Point out every malaria parasite.
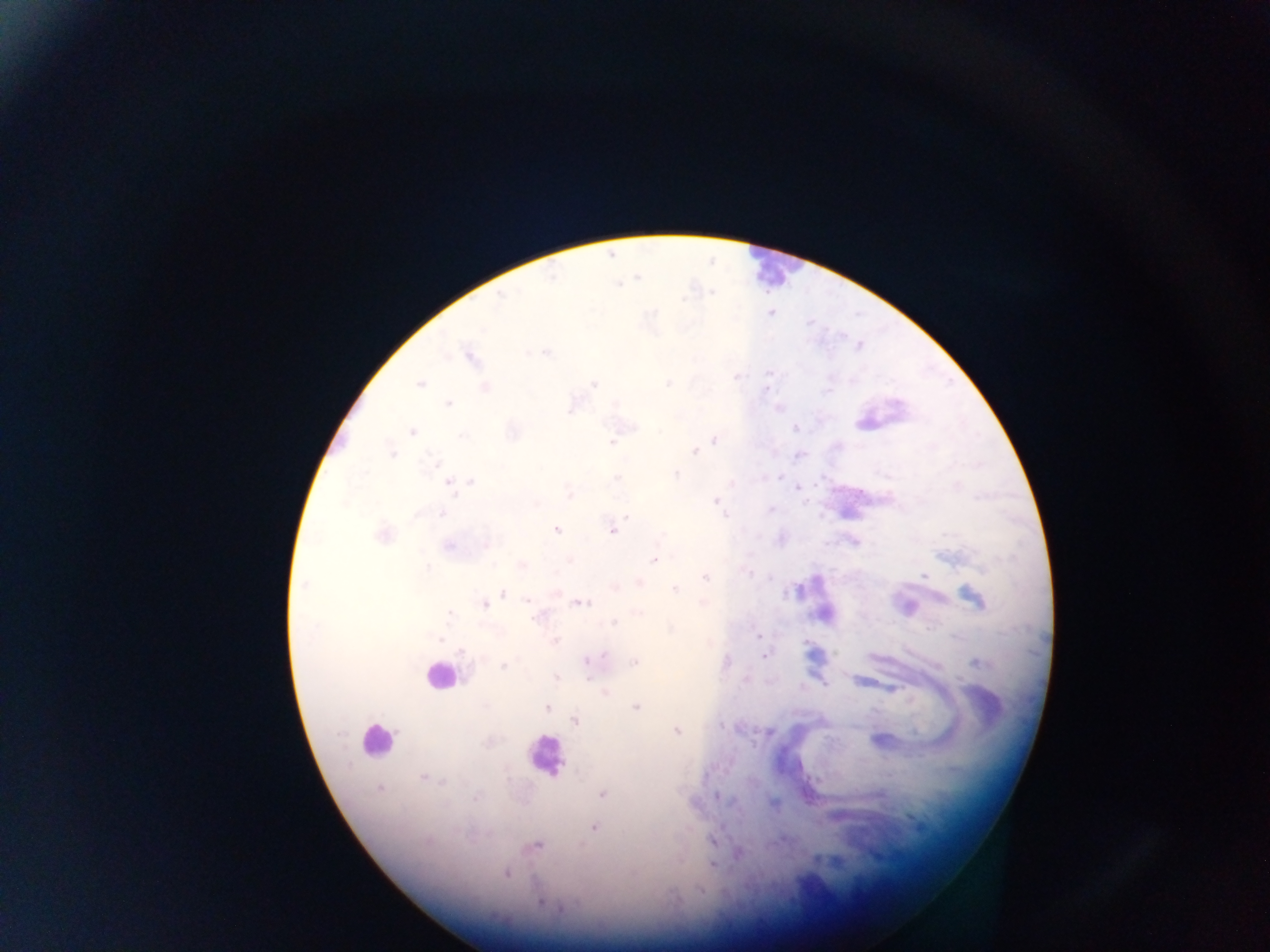

Approximate centers as x y in pixels.
Malaria parasites: 771 312; 470 356; 421 383; 669 383; 484 387; 448 403; 572 405; 412 431; 614 439; 714 439; 694 450; 390 453; 798 454; 450 482; 797 487; 716 502; 556 529; 613 529; 381 534; 855 541; 449 545; 655 558; 521 565; 924 574; 705 576; 638 583; 675 588; 503 593; 973 598; 580 603; 485 604; 906 608; 824 614; 614 622; 759 636; 555 640; 765 655; 636 662; 557 679; 605 694; 546 707; 636 707; 575 719; 676 731; 881 740; 379 788; 603 794; 717 796; 594 827; 536 845; 737 852; 712 864; 506 873; 701 891.

{
  "field_of_view": "single",
  "preparation": "thick blood film",
  "country": "Ghana",
  "image_size": "1270×952 pixels",
  "leukocyte_locations": "approximate centers as x y in pixels: 773 269; 439 675; 377 740; 546 756",
  "capture": "mobile-phone photograph through a microscope"
}